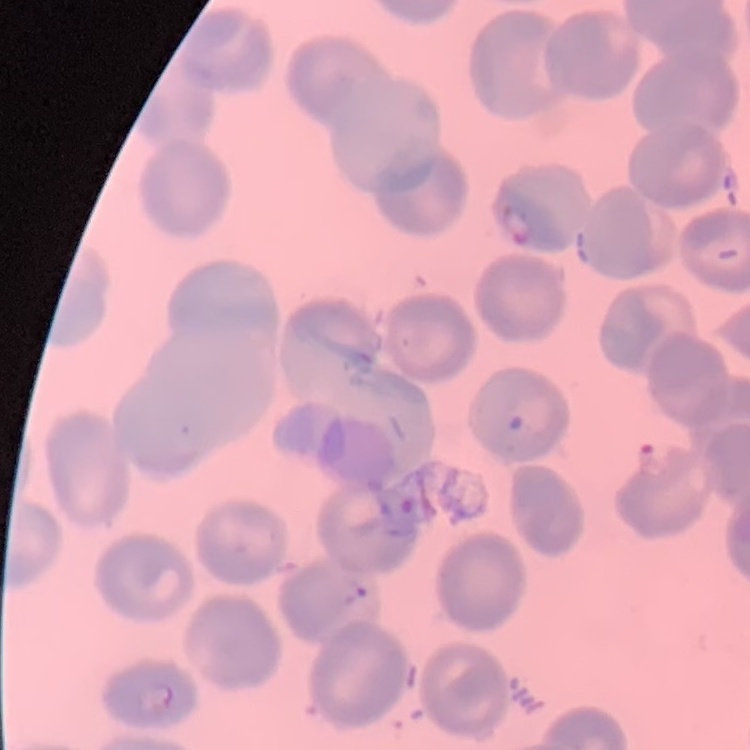
Summary:
  - Erythrocyte morphology: no rouleaux formation
  - Preparation: thin blood film
  - Image type: one tile cut from a larger photomicrograph
  - Stain: Field's or Giemsa